Point out each Plasmodium parasite.
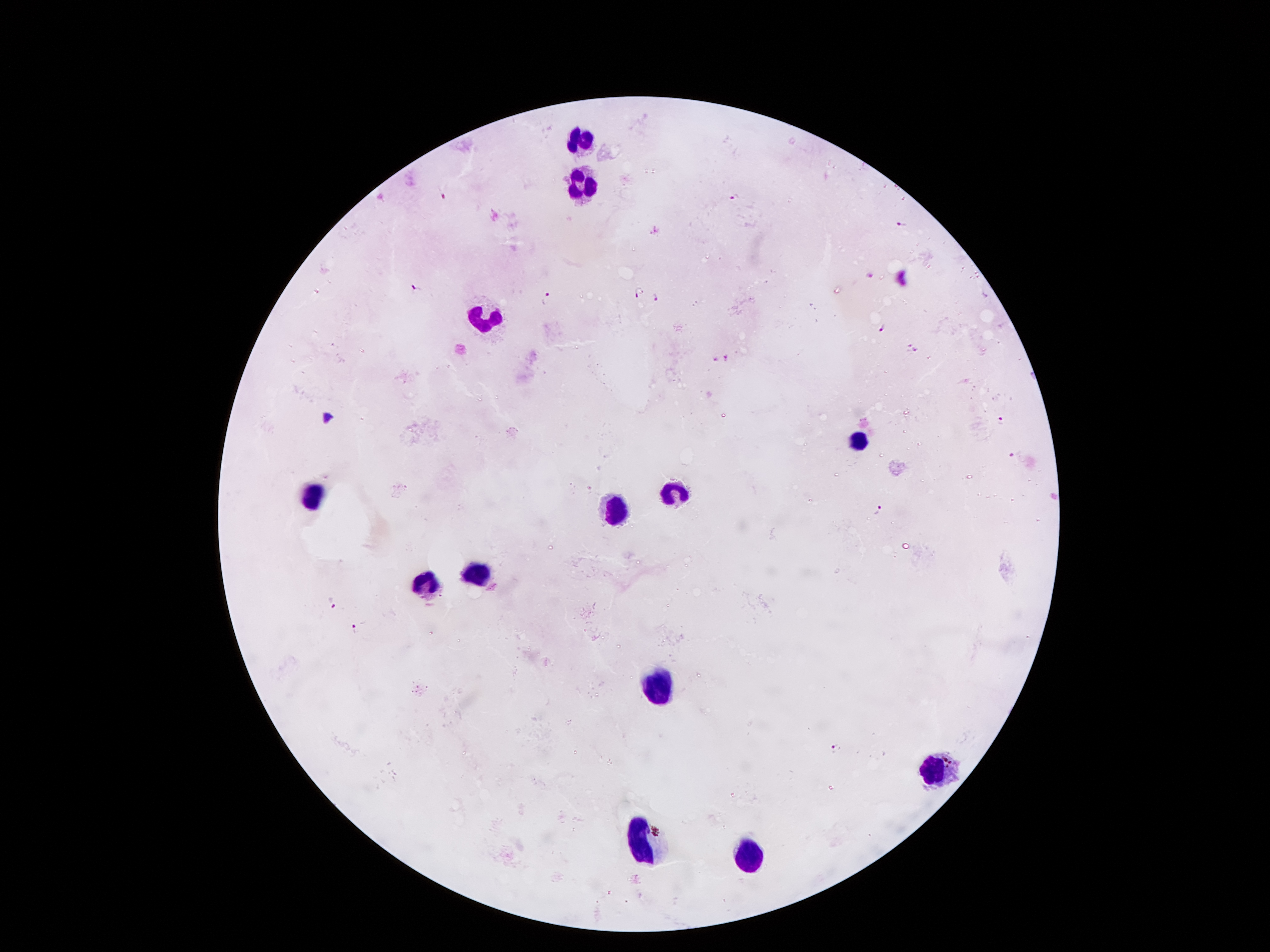
Approximate centers as (x, y) in pixels.
Plasmodium parasites: (446, 194), (733, 197), (902, 225), (870, 277), (417, 288), (639, 291), (656, 297), (546, 299), (881, 328), (908, 344), (915, 351), (727, 356), (715, 358), (1003, 421), (1012, 454), (878, 511), (335, 603), (355, 627), (835, 748).

Summary:
  - Leukocyte locations: (582, 141), (587, 182), (484, 318), (859, 437), (671, 491), (312, 498), (618, 509), (473, 570), (428, 582), (655, 686), (932, 774), (641, 848), (746, 856)
  - Image size: 1270×952 pixels
  - Stain: Giemsa
  - Preparation: thick peripheral-blood smear
  - Capture: smartphone through the microscope eyepiece
  - Magnification: 100x
  - Field of view: one from this slide
  - Patient malaria status: positive for Plasmodium falciparum